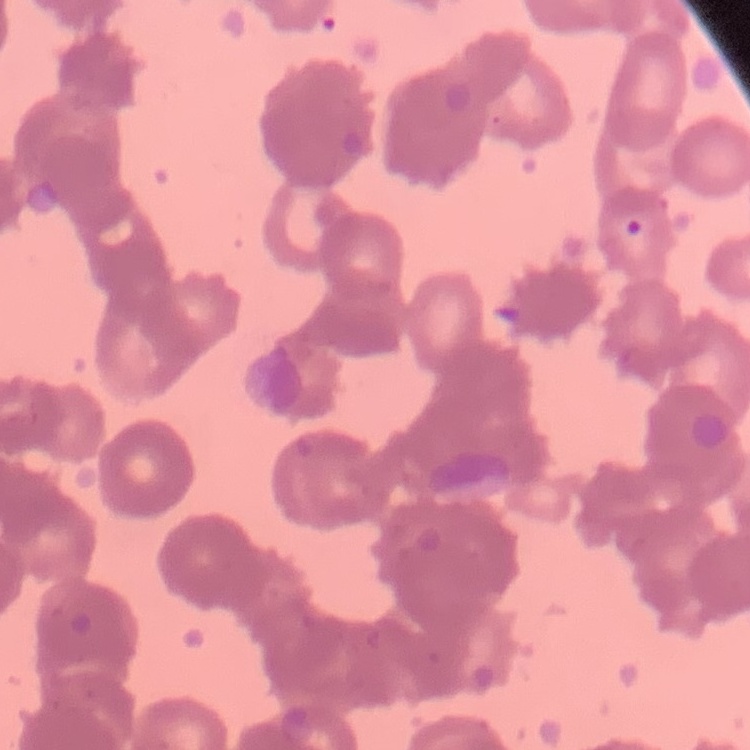

Summary:
  - Erythrocyte morphology: rouleaux formation
  - Preparation: thin peripheral smear
  - Stain: Field's or Giemsa
  - Image type: one tile cut from a larger photomicrograph